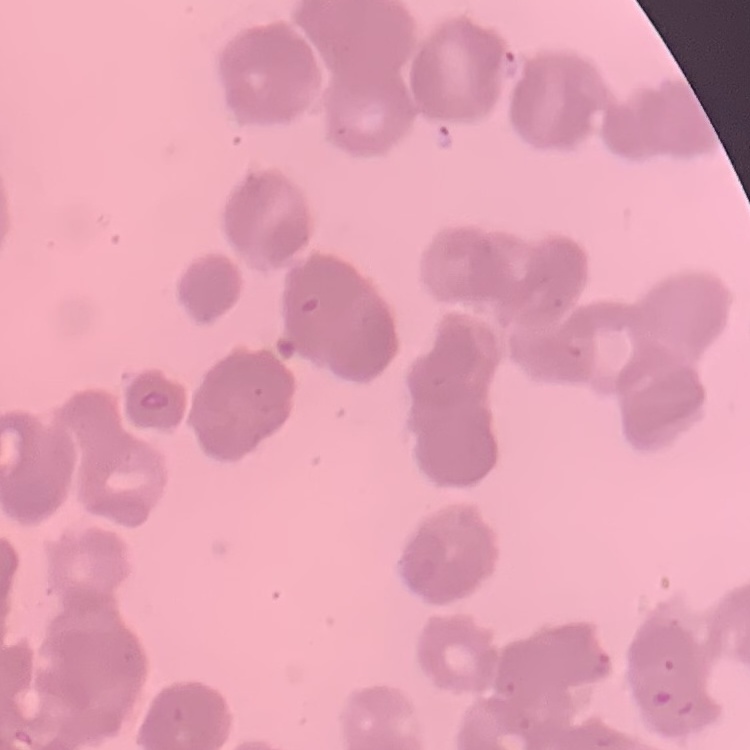
Summary:
  - Red blood cell morphology: rouleaux formation
  - Stain: Field's or Giemsa
  - Preparation: thin blood film
  - Image type: square crop of a larger photomicrograph